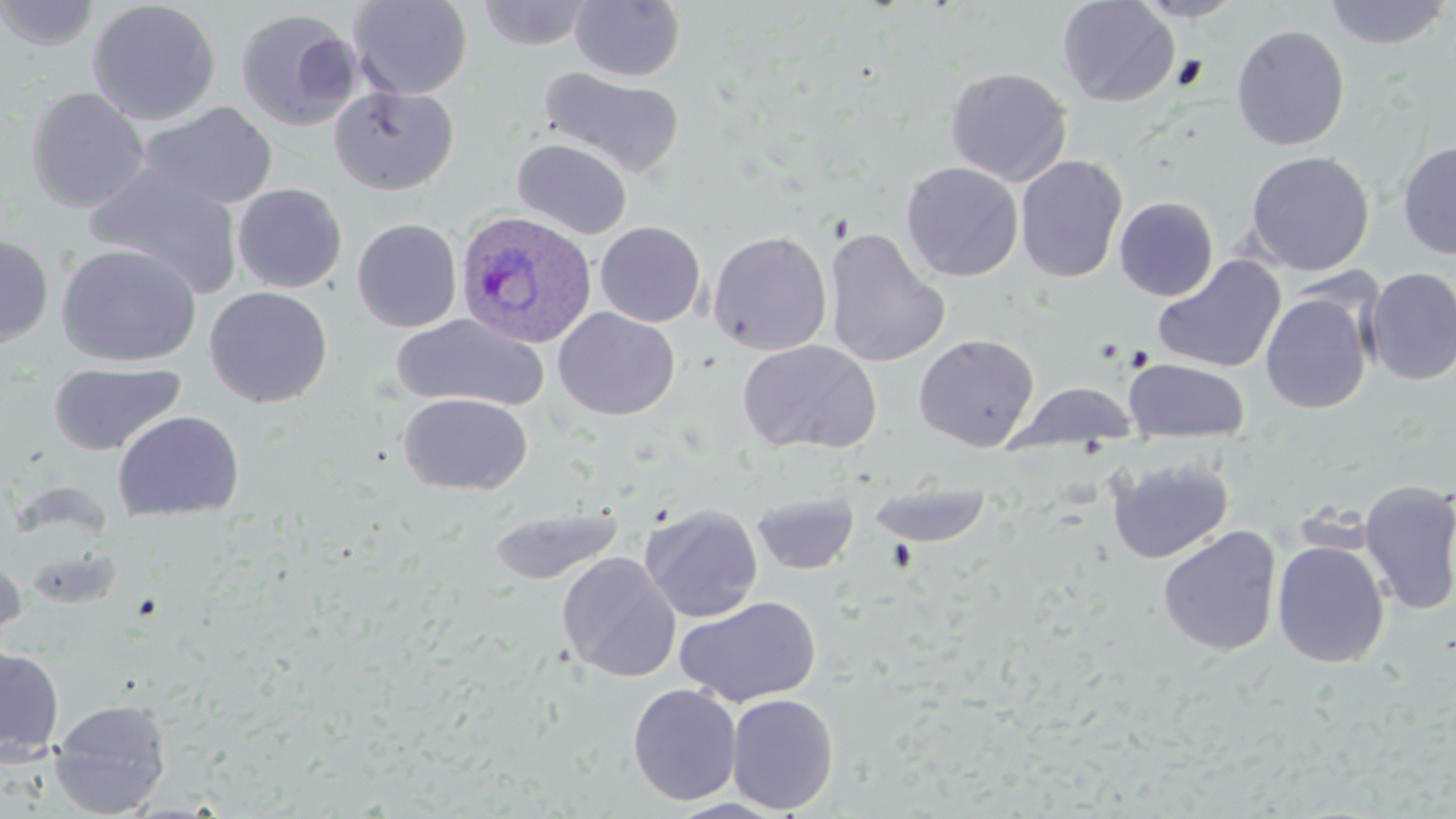
{
  "slide_level_diagnosis": "Plasmodium ovale",
  "field_of_view": "one of a larger specimen",
  "preparation": "thin blood smear",
  "image_size": "1456×819 pixels",
  "uninfected_red_blood_cell_locations": "approximate bounding boxes as (x1, y1, x2, y2) in pixels: (0, 0, 102, 51), (348, 0, 473, 99), (569, 0, 686, 82), (1130, 0, 1247, 22), (1323, 0, 1454, 49), (87, 1, 221, 125), (476, 1, 593, 50), (1057, 1, 1180, 107), (235, 7, 363, 131), (1231, 24, 1350, 151), (539, 66, 685, 180), (945, 67, 1072, 186), (329, 85, 460, 196), (25, 87, 150, 212), (138, 102, 278, 211), (511, 138, 633, 240), (1396, 139, 1456, 261), (1244, 150, 1375, 275), (1014, 155, 1127, 284), (901, 162, 1023, 281), (86, 163, 244, 300), (232, 183, 346, 292), (1115, 196, 1218, 301), (352, 218, 462, 333), (595, 221, 706, 327), (824, 227, 948, 368), (708, 230, 832, 356), (0, 234, 53, 347), (56, 243, 202, 367), (1152, 255, 1286, 373), (1362, 267, 1456, 385), (204, 286, 332, 408), (1260, 291, 1374, 414), (553, 307, 680, 420), (392, 313, 550, 410), (913, 333, 1039, 452), (736, 340, 881, 455), (1123, 358, 1251, 442), (47, 361, 187, 456), (1010, 381, 1140, 453), (398, 393, 532, 495), (112, 410, 245, 521), (1106, 457, 1234, 564), (1358, 479, 1456, 616), (867, 482, 992, 547), (751, 492, 859, 575), (640, 503, 763, 623), (488, 505, 623, 585), (1157, 525, 1282, 657), (1272, 540, 1390, 668), (0, 553, 27, 654), (557, 553, 681, 682), (675, 596, 821, 708), (0, 645, 64, 763), (628, 683, 742, 805), (726, 693, 839, 814), (49, 697, 172, 816)",
  "stain": "May-Grünwald-Giemsa",
  "modality": "light microscopy",
  "plasmodium_ovale_infected_red_blood_cell_locations": "approximate bounding boxes as (x1, y1, x2, y2) in pixels: (455, 211, 597, 349)",
  "magnification": "1000x"
}